Report the malaria status of this cell.
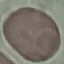
It is uninfected.

Giemsa stain. Thin blood smear. Cell patch, automatically extracted from a larger field of view and resized to 64 × 64 pixels. Photographed with a smartphone camera at the microscope eyepiece.